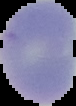 Segmented cell region on a black background. Image is 76×106 pixels. Malaria status: uninfected. From a thin blood smear.